Describe the morphology of the erythrocytes.
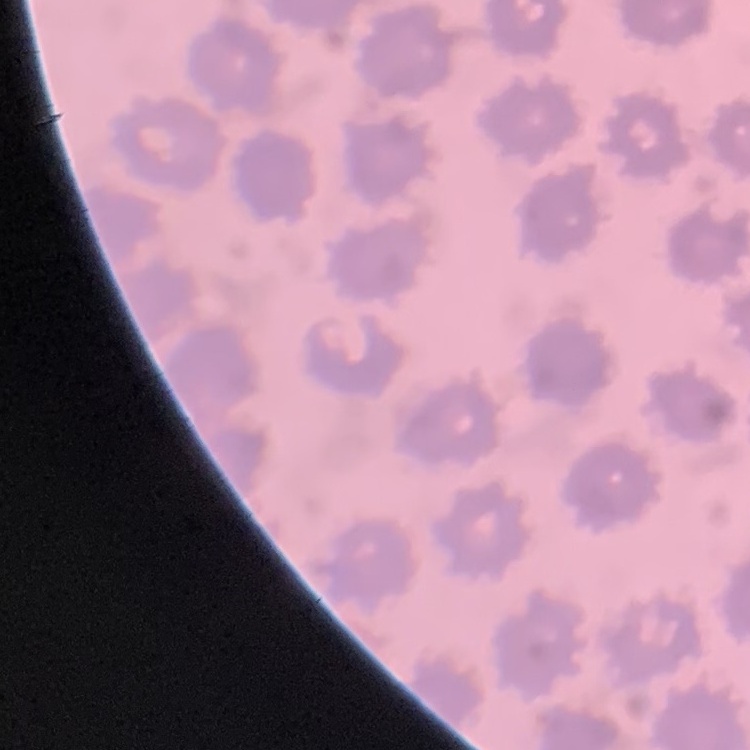
They show no rouleaux formation.

Summary:
  - Stain: Field's or Giemsa
  - Preparation: thin blood film
  - Image type: square crop of a larger photomicrograph